Give the preparation type.
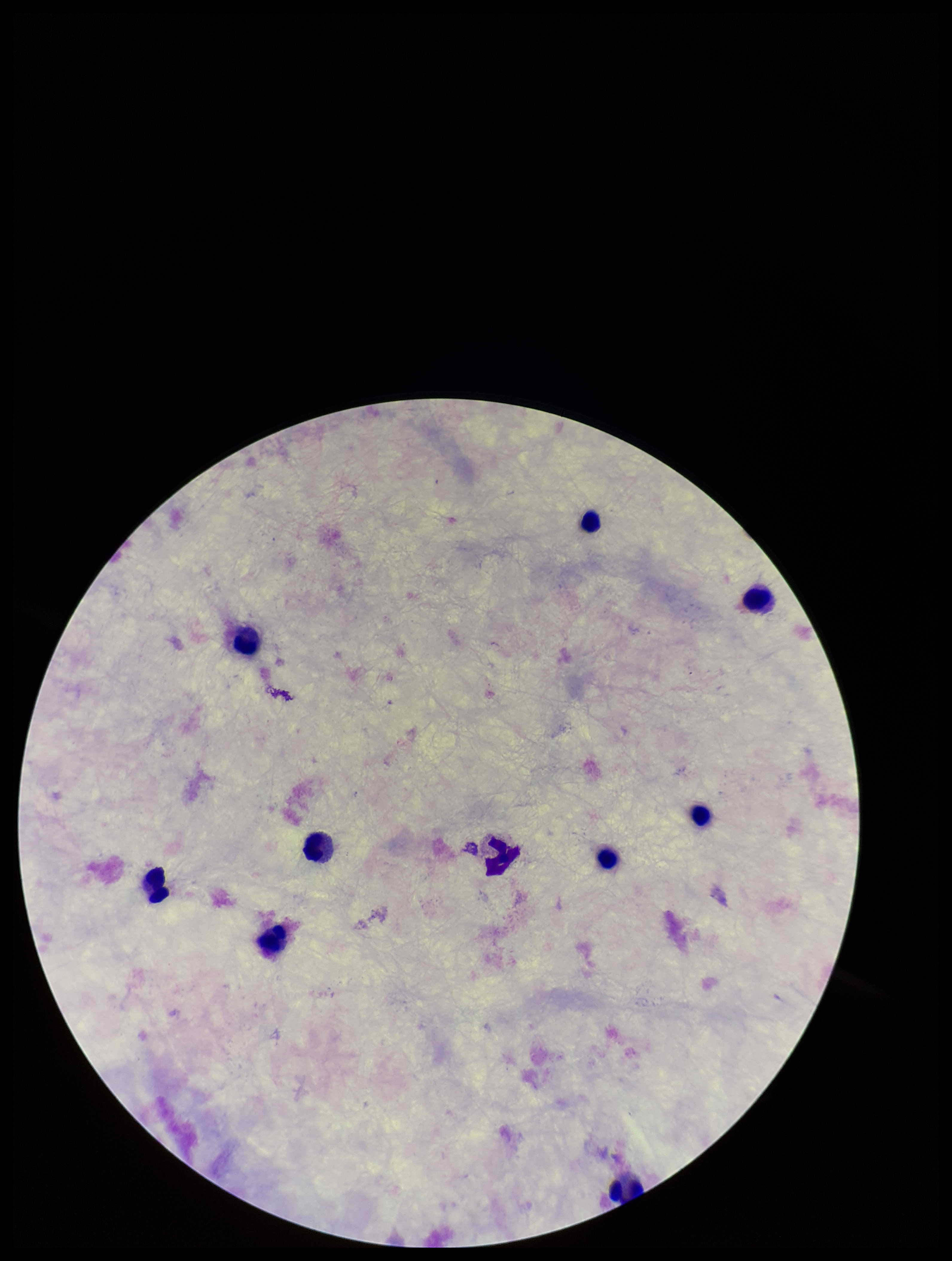

Thick.

Patient malaria status: negative. Plasmodium parasites: none identified. Image is 952×1261 pixels. Photographed through the microscope eyepiece with a smartphone camera. Parasite count: 0. Giemsa stain. One field from this slide. Leukocyte count: 9.